Look for parasitized red blood cells.
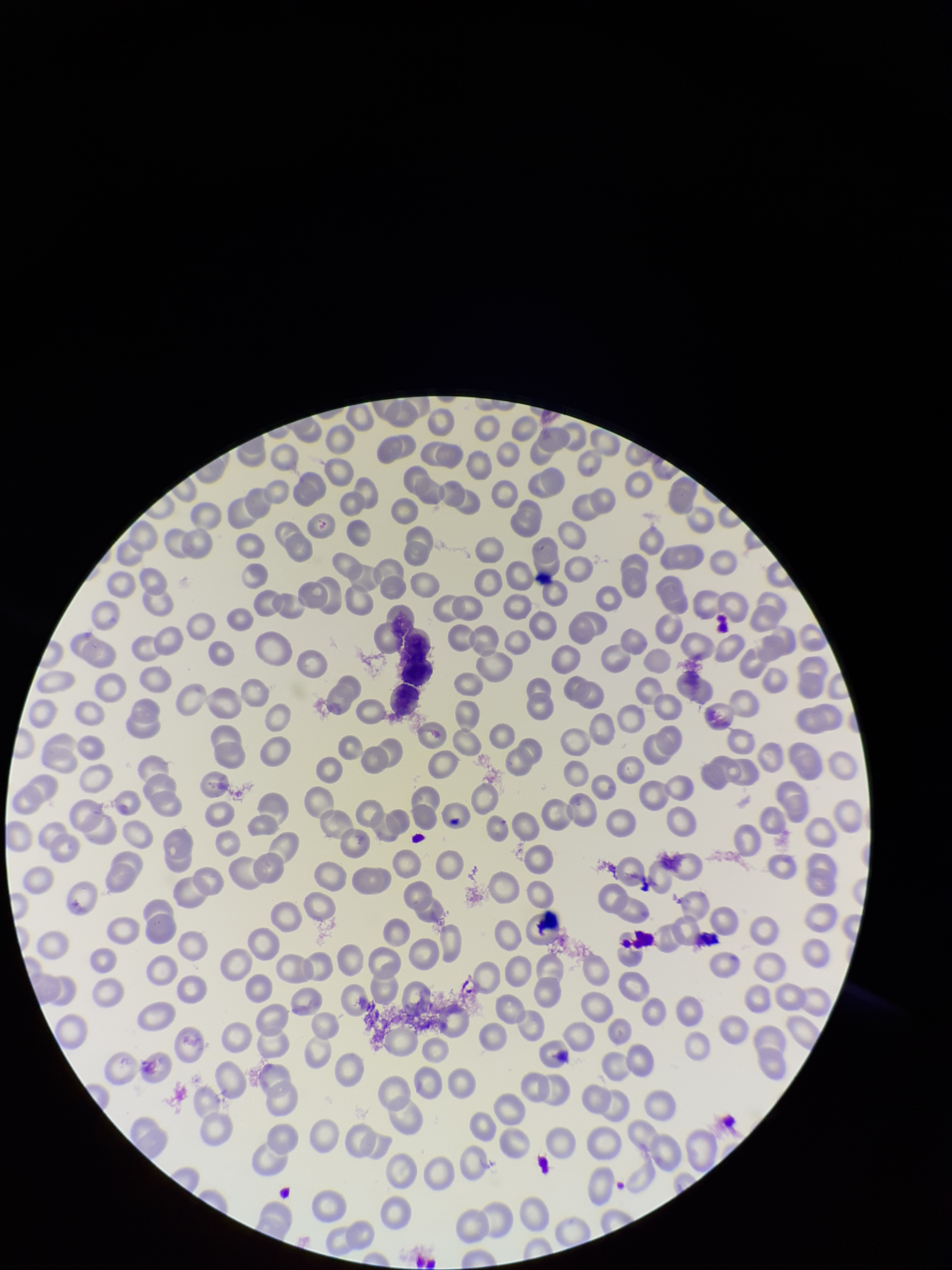

None detected.

parasitized red blood cell count = 0
capture = smartphone photograph through the microscope eyepiece
image size = 952×1270 pixels
preparation = thin
field of view = single
patient malaria status = negative
stain = Giemsa
red blood cell count = 278